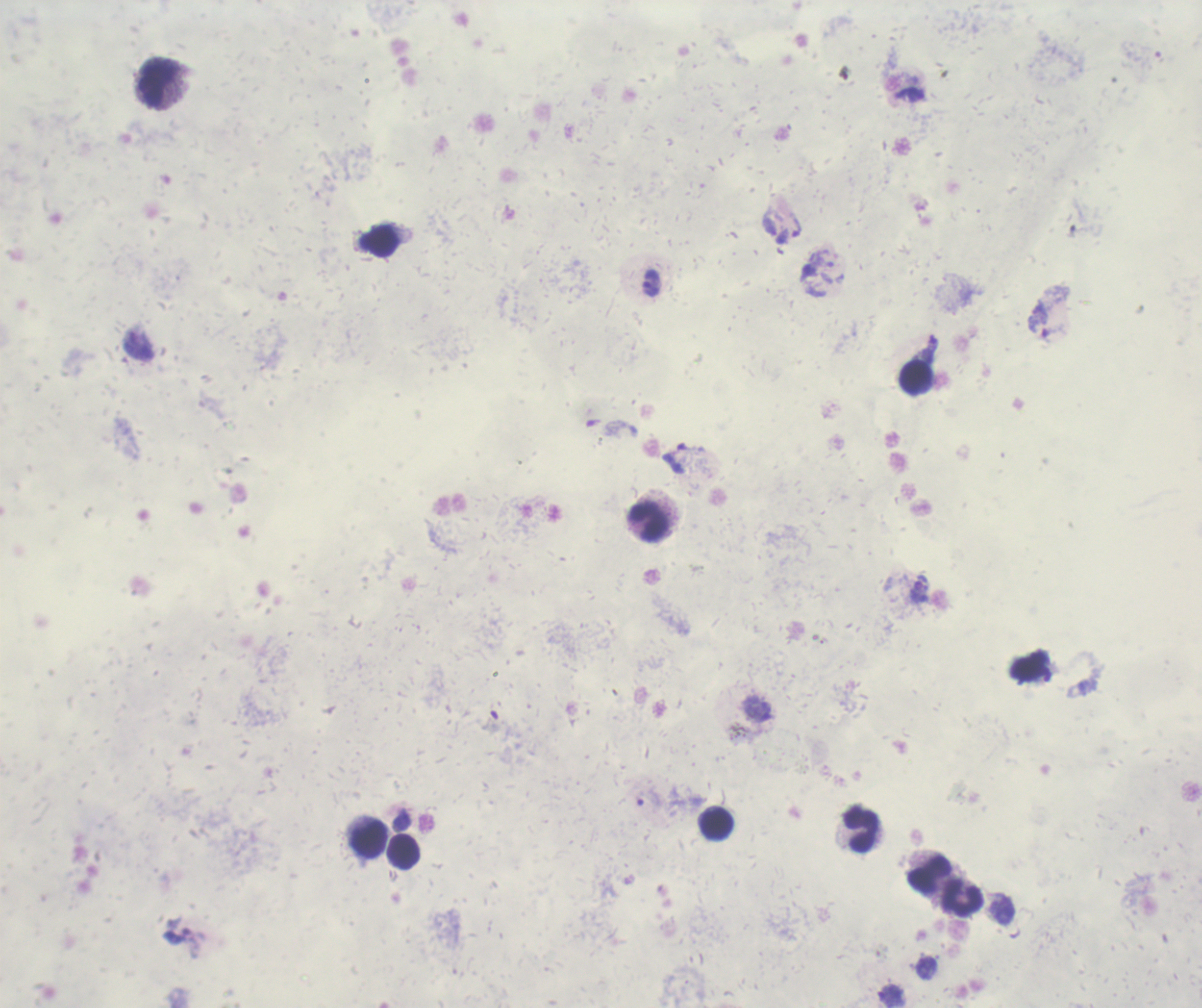
Approximate centers as [x, y] in pixels. Trophozoite locations: [824, 267], [651, 282], [1038, 319], [139, 345]. Leukocyte locations: [157, 84], [380, 242], [916, 377], [649, 522], [715, 823], [861, 830], [368, 839], [404, 852], [928, 874], [963, 899]. Romanowsky stain. Result: positive for Plasmodium parasites. Image is 1202×1008 pixels. Background quality: poor. Previously used in a real diagnosis. Thick blood film. Coloration quality: bad. One field from this slide. 100x magnification.